Outline each uninfected red blood cell.
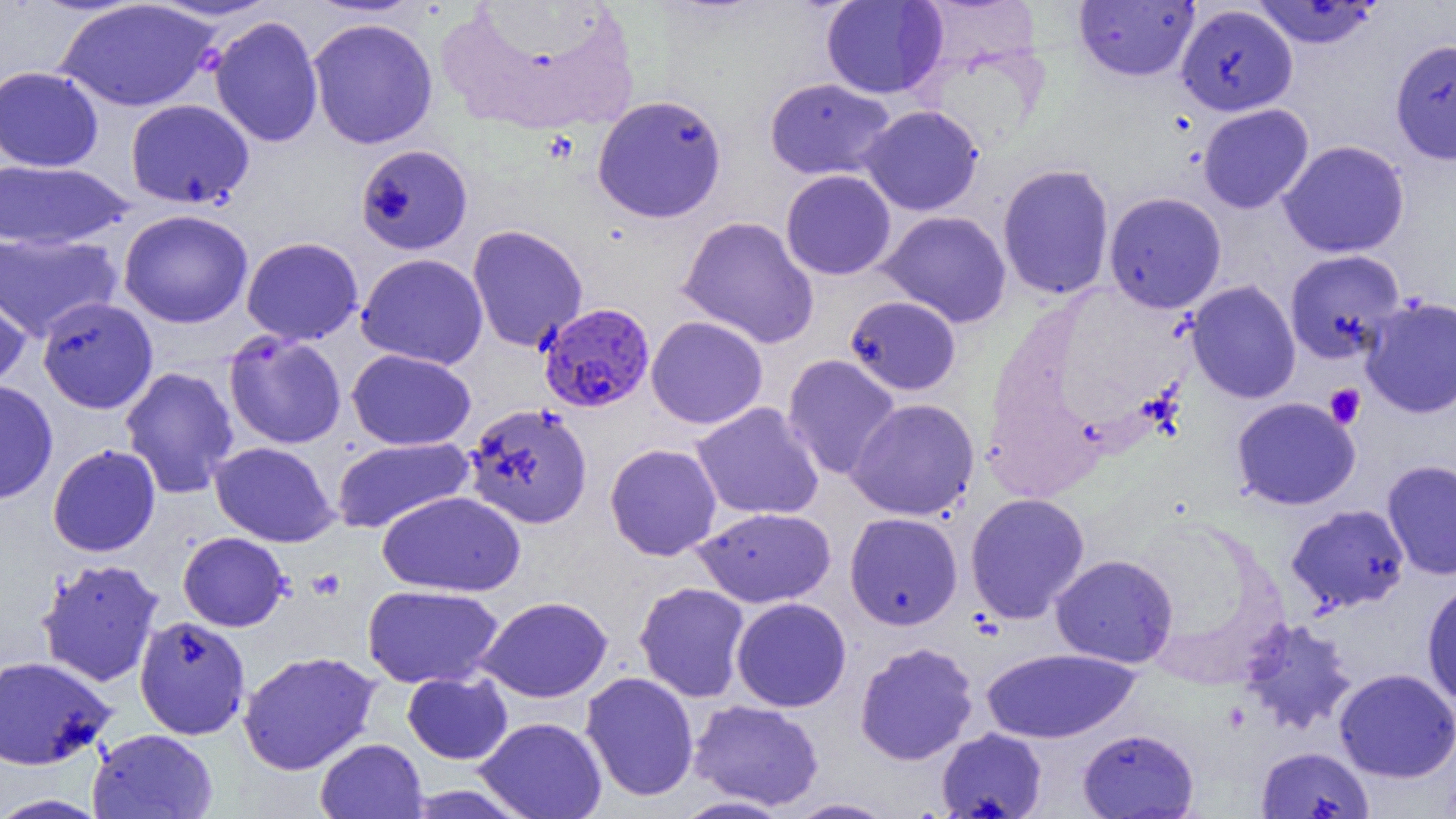

Approximate bounding boxes as [x1, y1, x2, y2] in pixels.
Uninfected red blood cells: [146, 0, 283, 22], [821, 0, 948, 99], [56, 1, 220, 112], [1074, 1, 1199, 81], [1251, 1, 1383, 48], [1176, 3, 1298, 116], [208, 15, 324, 148], [307, 17, 438, 149], [1390, 38, 1456, 165], [0, 66, 104, 172], [764, 77, 897, 180], [591, 94, 727, 223], [125, 98, 254, 209], [1197, 104, 1314, 213], [858, 105, 983, 216], [1278, 140, 1410, 258], [355, 144, 472, 255], [0, 159, 134, 251], [997, 163, 1115, 300], [780, 169, 897, 280], [1104, 191, 1227, 314], [118, 209, 253, 328], [877, 210, 1012, 327], [678, 215, 820, 349], [467, 224, 588, 352], [0, 231, 122, 342], [241, 237, 364, 345], [1284, 250, 1405, 364], [356, 253, 488, 370], [1185, 280, 1301, 404], [0, 282, 31, 391], [844, 295, 962, 396], [1360, 296, 1456, 419], [37, 297, 159, 414], [646, 315, 768, 429], [223, 332, 347, 450], [347, 349, 476, 450], [782, 354, 901, 481], [119, 366, 240, 498], [0, 380, 59, 505], [1231, 397, 1360, 510], [846, 398, 980, 521], [691, 402, 825, 521], [464, 403, 593, 529], [331, 436, 475, 535], [210, 441, 338, 547], [604, 443, 722, 561], [47, 444, 161, 557], [1381, 459, 1456, 580], [1321, 480, 1456, 607], [378, 491, 524, 596], [965, 493, 1090, 623], [1286, 504, 1410, 614], [694, 507, 835, 608], [844, 512, 963, 630], [177, 532, 290, 632], [1050, 554, 1178, 668], [35, 558, 165, 687], [1421, 579, 1456, 707], [633, 581, 751, 703], [362, 584, 504, 689], [476, 596, 613, 702], [731, 597, 851, 712], [134, 616, 251, 740], [1237, 616, 1358, 735], [854, 642, 979, 765], [980, 647, 1138, 743], [238, 650, 380, 775], [0, 655, 116, 770], [1333, 668, 1456, 782], [402, 671, 513, 764], [580, 671, 699, 802], [689, 700, 824, 810], [474, 717, 608, 819], [88, 728, 218, 819], [936, 728, 1047, 819], [1078, 728, 1199, 818], [314, 738, 428, 819], [1256, 746, 1374, 819], [400, 784, 535, 818], [0, 793, 111, 818], [671, 795, 793, 818], [784, 798, 898, 818].

Summary:
  - Plasmodium falciparum-infected red blood cell locations: [538, 302, 655, 413]
  - Platelet locations: [1324, 383, 1366, 428], [308, 568, 347, 601]
  - Slide-level diagnosis: Plasmodium falciparum
  - Preparation: thin blood smear
  - Magnification: 1000x
  - Image size: 1456×819 pixels
  - Field of view: single
  - Modality: optical microscopy